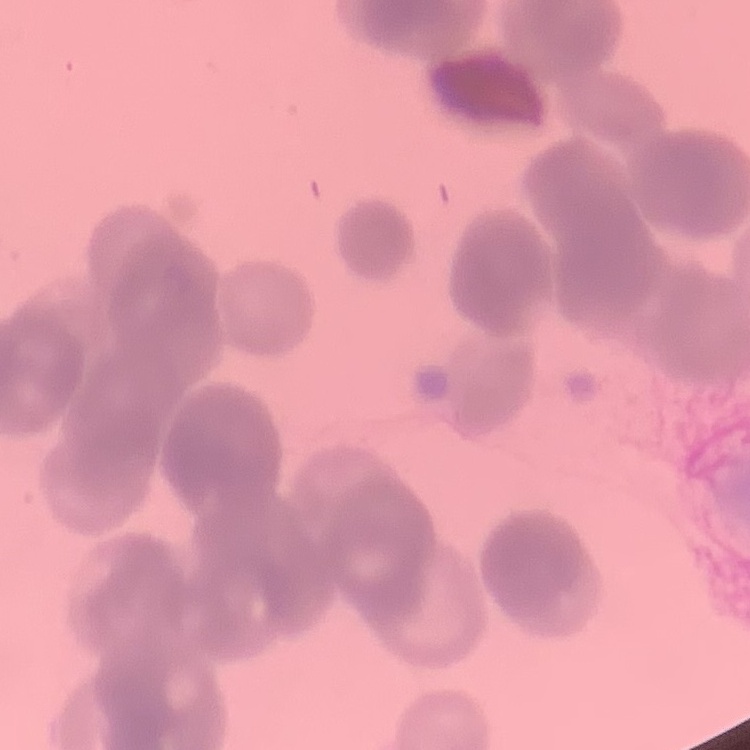

erythrocyte_morphology: rouleaux formation
image_type: one tile cut from a larger photomicrograph
preparation: thin blood film
stain: Field's or Giemsa